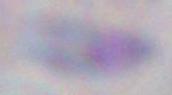

Summary:
  - Identification: Toxoplasma gondii
  - Magnification: 1000x
  - Modality: micrograph